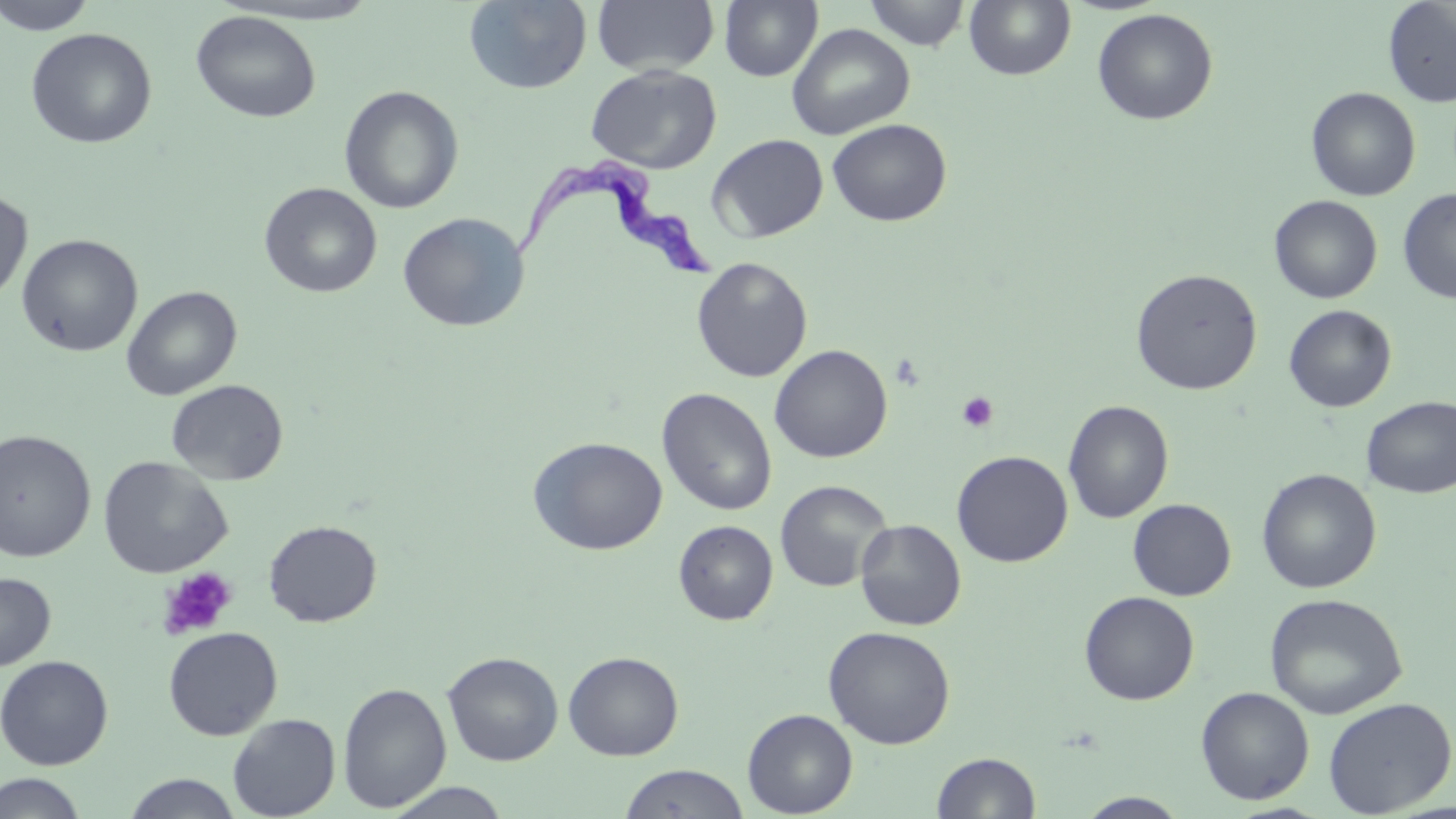
Summary:
  - Coordinate format: approximate bounding boxes as [x1, y1, x2, y2] in pixels
  - Platelet locations: [957, 391, 999, 433], [158, 567, 238, 641]
  - Uninfected red blood cell locations: [1, 0, 98, 35], [464, 0, 592, 95], [592, 0, 719, 76], [720, 0, 822, 82], [863, 0, 971, 50], [964, 1, 1076, 81], [1383, 1, 1456, 107], [1091, 8, 1219, 126], [190, 10, 321, 123], [787, 23, 915, 140], [25, 27, 157, 149], [585, 65, 721, 174], [339, 85, 464, 214], [1305, 87, 1420, 201], [827, 118, 952, 226], [708, 134, 829, 243], [259, 182, 382, 298], [1398, 188, 1456, 303], [0, 189, 33, 306], [1268, 195, 1383, 304], [398, 212, 530, 332], [16, 234, 143, 357], [691, 257, 813, 383], [1131, 268, 1263, 395], [121, 286, 242, 400], [1284, 305, 1397, 413], [769, 344, 892, 463], [166, 379, 289, 485], [657, 387, 777, 516], [1361, 396, 1456, 498], [1063, 399, 1174, 523], [0, 429, 96, 562], [528, 436, 667, 556], [952, 450, 1073, 567], [98, 456, 233, 578], [1256, 468, 1382, 594], [775, 479, 892, 592], [1127, 499, 1236, 601], [855, 519, 966, 631], [264, 520, 382, 627], [673, 520, 778, 624], [0, 572, 56, 670], [1079, 591, 1199, 705], [1264, 592, 1408, 719], [822, 625, 955, 749], [163, 626, 282, 740], [442, 651, 564, 765], [563, 651, 684, 761], [0, 655, 114, 770], [337, 682, 451, 813], [1195, 686, 1315, 805], [1322, 697, 1455, 816], [742, 708, 857, 817], [227, 713, 340, 818], [931, 752, 1041, 818], [618, 764, 750, 819], [0, 772, 90, 818], [122, 773, 243, 818], [384, 783, 513, 819], [1076, 792, 1191, 818]
  - Trypanosoma brucei locations: [510, 157, 724, 281]
  - Slide-level diagnosis: Trypanosoma brucei
  - Image size: 1456×819 pixels
  - Stain: May-Grünwald-Giemsa
  - Magnification: 1000x
  - Modality: optical microscopy
  - Preparation: thin blood smear
  - Field of view: single